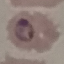
Result: malaria parasites detected. Giemsa-stained preparation. Cell patch, automatically extracted from a larger field of view and resized to 64 × 64 pixels. Thin blood film. Acquired by smartphone through the microscope eyepiece.